Identify the cell.
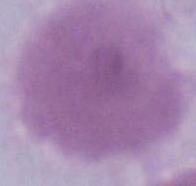

An erythrocyte.

Micrograph. 1000x magnification.